Name the parasite shown.
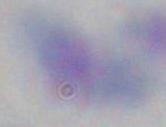

This is Toxoplasma gondii.

Micrograph. Captured at 1000x magnification.